Identify the blood parasite species.
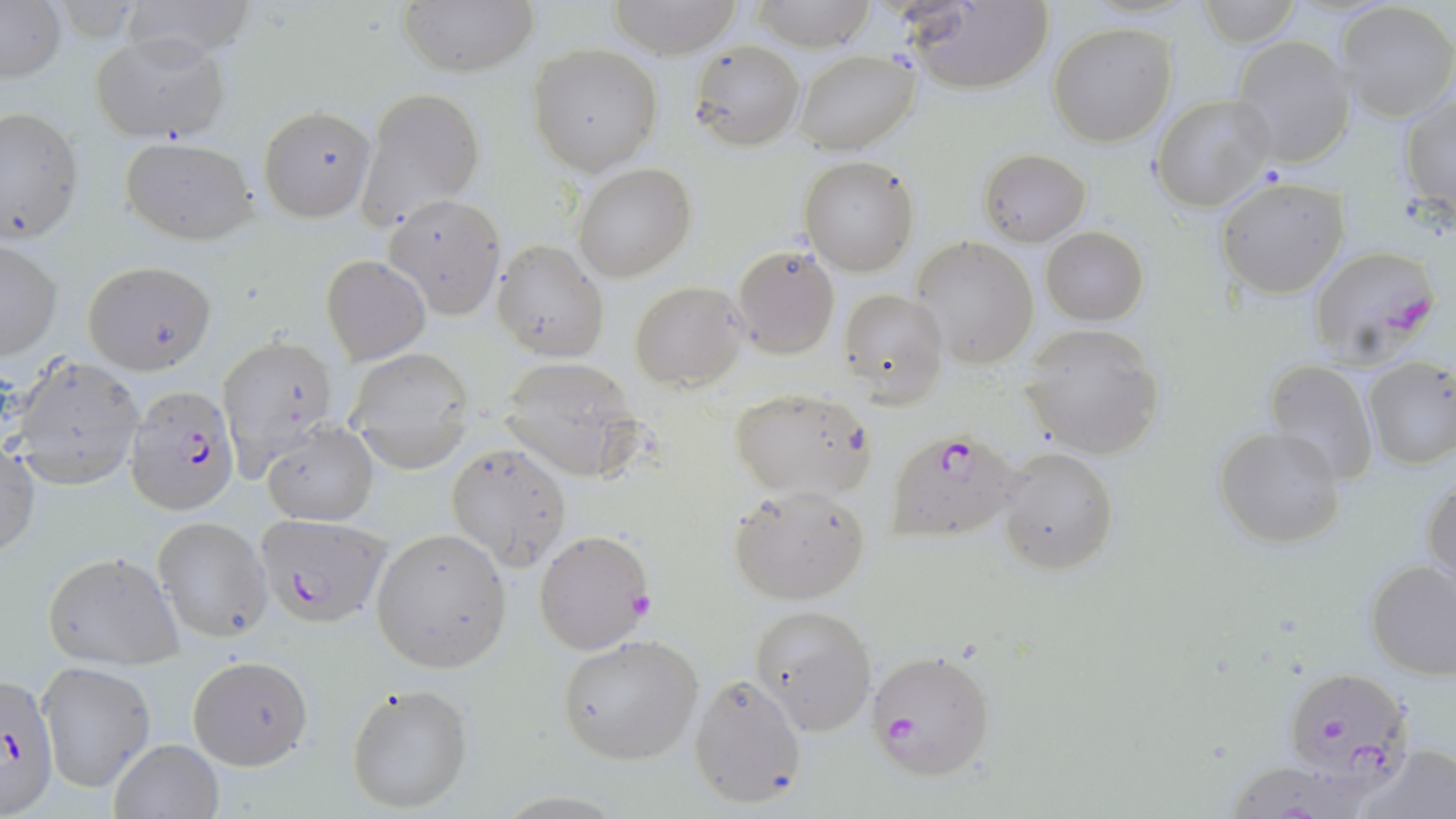
Plasmodium falciparum.

{
  "magnification": "1000x",
  "stain": "May-Grünwald-Giemsa",
  "modality": "optical microscopy",
  "uninfected_red_blood_cell_locations": "approximate bounding boxes as (x1,y1)-(x2,y2) corner pairs in pixels: (118,0)-(259,64), (396,0)-(538,77), (607,0)-(743,58), (749,0)-(877,50), (1196,1)-(1303,46), (0,2)-(65,84), (904,3)-(1051,93), (1337,3)-(1455,122), (1048,22)-(1177,146), (89,31)-(230,140), (1232,36)-(1355,168), (689,39)-(805,152), (528,43)-(663,175), (793,49)-(920,156), (360,88)-(484,225), (1151,94)-(1277,212), (1399,94)-(1456,211), (0,105)-(83,246), (257,105)-(376,221), (119,136)-(258,244), (979,147)-(1090,245), (800,156)-(919,276), (573,164)-(694,282), (1215,176)-(1348,299), (382,194)-(506,318), (1041,227)-(1148,326), (912,237)-(1039,369), (0,239)-(62,359), (492,239)-(608,361), (731,245)-(839,359), (321,254)-(430,364), (82,260)-(216,374), (629,281)-(746,390), (839,287)-(948,407), (1021,324)-(1163,458), (225,336)-(338,485), (344,346)-(475,471), (5,352)-(145,483), (497,356)-(643,479), (1362,357)-(1456,470), (1263,361)-(1379,485), (726,389)-(876,499), (261,421)-(376,527), (1214,424)-(1348,549), (446,442)-(572,571), (997,446)-(1119,575), (0,447)-(40,562), (1423,474)-(1455,592), (726,483)-(870,605), (152,517)-(271,642), (371,528)-(512,673), (44,551)-(183,670), (1365,558)-(1456,677), (750,604)-(876,735), (556,633)-(704,765), (188,654)-(313,769), (36,662)-(154,792), (688,673)-(807,808), (345,682)-(474,814), (108,737)-(223,819), (1357,743)-(1456,819)",
  "plasmodium_falciparum_infected_red_blood_cell_locations": "approximate bounding boxes as (x1,y1)-(x2,y2) corner pairs in pixels: (1306,244)-(1441,362), (128,385)-(240,516), (886,426)-(1025,544), (254,513)-(389,628), (534,529)-(653,653), (865,648)-(994,781), (1281,666)-(1417,786), (0,675)-(60,815), (1235,766)-(1361,819)",
  "field_of_view": "one of a larger specimen",
  "image_size": "1456×819 pixels",
  "preparation": "thin blood smear"
}